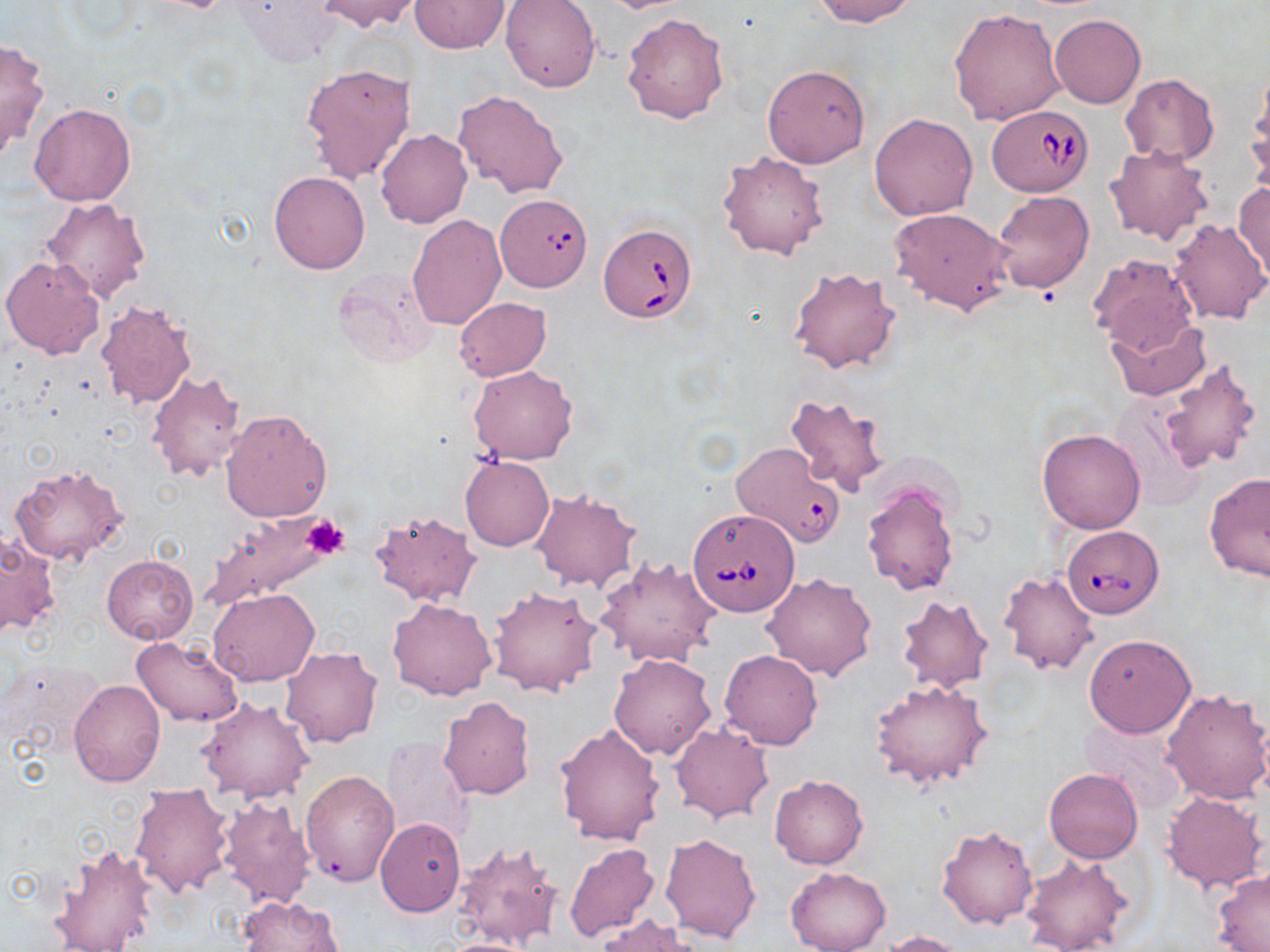
Approximate bounding boxes as named x1/y1/x2/y2 corners in pixels. Uninfected red blood cell locations: (x1=233, y1=0, x2=344, y2=67), (x1=314, y1=0, x2=420, y2=33), (x1=410, y1=0, x2=511, y2=54), (x1=500, y1=0, x2=599, y2=92), (x1=809, y1=0, x2=919, y2=26), (x1=947, y1=8, x2=1065, y2=128), (x1=622, y1=13, x2=729, y2=123), (x1=1050, y1=13, x2=1146, y2=108), (x1=0, y1=37, x2=49, y2=160), (x1=300, y1=62, x2=416, y2=183), (x1=763, y1=64, x2=871, y2=167), (x1=1121, y1=73, x2=1218, y2=165), (x1=1245, y1=80, x2=1269, y2=194), (x1=453, y1=89, x2=568, y2=198), (x1=29, y1=104, x2=136, y2=207), (x1=869, y1=112, x2=978, y2=221), (x1=375, y1=129, x2=472, y2=228), (x1=1104, y1=145, x2=1214, y2=247), (x1=718, y1=150, x2=828, y2=260), (x1=269, y1=170, x2=370, y2=273), (x1=1232, y1=181, x2=1269, y2=282), (x1=993, y1=191, x2=1094, y2=292), (x1=41, y1=197, x2=151, y2=303), (x1=889, y1=207, x2=1013, y2=316), (x1=406, y1=215, x2=506, y2=331), (x1=1167, y1=218, x2=1269, y2=325), (x1=1088, y1=253, x2=1199, y2=355), (x1=2, y1=255, x2=106, y2=359), (x1=332, y1=264, x2=441, y2=368), (x1=788, y1=267, x2=902, y2=373), (x1=454, y1=297, x2=551, y2=381), (x1=95, y1=299, x2=198, y2=408), (x1=1105, y1=314, x2=1208, y2=400), (x1=1158, y1=359, x2=1265, y2=475), (x1=469, y1=365, x2=578, y2=464), (x1=146, y1=369, x2=248, y2=483), (x1=785, y1=394, x2=892, y2=495), (x1=220, y1=408, x2=334, y2=523), (x1=1036, y1=427, x2=1146, y2=534), (x1=460, y1=456, x2=554, y2=551), (x1=9, y1=462, x2=131, y2=566), (x1=1203, y1=473, x2=1270, y2=583), (x1=861, y1=479, x2=959, y2=597), (x1=530, y1=489, x2=641, y2=592), (x1=199, y1=511, x2=345, y2=612), (x1=370, y1=511, x2=479, y2=606), (x1=0, y1=532, x2=60, y2=637), (x1=101, y1=553, x2=198, y2=645), (x1=595, y1=556, x2=719, y2=666), (x1=998, y1=570, x2=1099, y2=676), (x1=760, y1=572, x2=877, y2=681), (x1=488, y1=585, x2=604, y2=698), (x1=208, y1=589, x2=319, y2=687), (x1=896, y1=593, x2=994, y2=693), (x1=385, y1=597, x2=497, y2=700), (x1=1083, y1=635, x2=1195, y2=739), (x1=131, y1=637, x2=245, y2=727), (x1=280, y1=647, x2=384, y2=748), (x1=719, y1=650, x2=823, y2=751), (x1=609, y1=653, x2=716, y2=760), (x1=871, y1=678, x2=993, y2=790), (x1=69, y1=679, x2=166, y2=788), (x1=1160, y1=686, x2=1270, y2=805), (x1=437, y1=696, x2=536, y2=801), (x1=198, y1=697, x2=314, y2=804), (x1=671, y1=721, x2=773, y2=823), (x1=554, y1=722, x2=667, y2=846), (x1=380, y1=738, x2=474, y2=845), (x1=1044, y1=768, x2=1142, y2=864), (x1=301, y1=769, x2=399, y2=886), (x1=769, y1=774, x2=868, y2=869), (x1=129, y1=784, x2=235, y2=898), (x1=1160, y1=790, x2=1267, y2=893), (x1=216, y1=798, x2=316, y2=909), (x1=375, y1=817, x2=465, y2=916), (x1=937, y1=824, x2=1039, y2=930), (x1=659, y1=832, x2=761, y2=942), (x1=455, y1=841, x2=563, y2=951), (x1=49, y1=842, x2=161, y2=952), (x1=563, y1=843, x2=660, y2=944), (x1=1020, y1=853, x2=1135, y2=952), (x1=786, y1=865, x2=891, y2=952), (x1=1212, y1=870, x2=1270, y2=950), (x1=237, y1=895, x2=345, y2=952), (x1=595, y1=915, x2=703, y2=952), (x1=881, y1=929, x2=971, y2=951), (x1=430, y1=936, x2=541, y2=952). Babesia divergens-infected red blood cell locations: (x1=988, y1=104, x2=1093, y2=197), (x1=498, y1=200, x2=594, y2=300), (x1=598, y1=224, x2=697, y2=322), (x1=730, y1=441, x2=846, y2=547), (x1=687, y1=507, x2=800, y2=617), (x1=1062, y1=525, x2=1165, y2=618). Platelet locations: (x1=303, y1=514, x2=349, y2=559). Slide-level diagnosis: Babesia divergens. Light microscopy. Image is 1270×952 pixels. Captured at 1000x magnification. One field of a larger specimen. Thin blood film. May-Grünwald-Giemsa-stained preparation.